Classify this cell by malaria status.
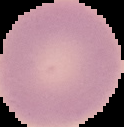

It is uninfected.

image_size: 124×127 pixels
preparation: thin blood smear
image_type: cell region segmented out of the field of view; surrounding area masked to black